State which parasite is depicted.
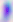
This is Toxoplasma gondii.

Summary:
  - Magnification: 400x
  - Modality: photomicrograph